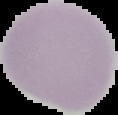

Summary:
  - Preparation: thin blood film
  - Malaria status: uninfected
  - Image size: 118×115 pixels
  - Image type: segmented cell region with the area outside set to black